Outline each blood parasite and name the species.
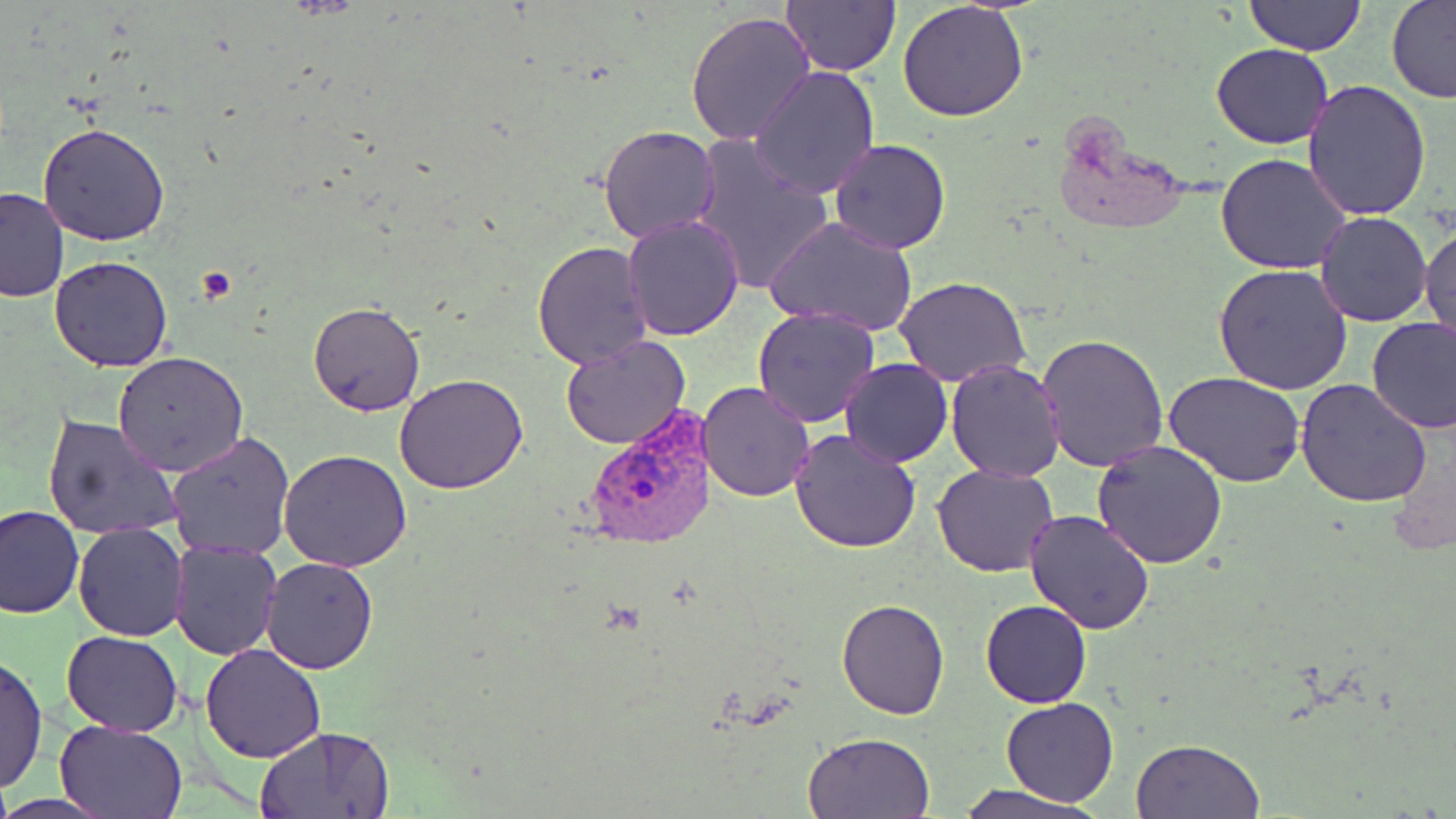
Approximate bounding boxes as [x1, y1, x2, y2] in pixels.
Plasmodium vivax-infected red blood cells: [581, 408, 720, 549].
No Plasmodium falciparum, Plasmodium ovale, Plasmodium malariae, Babesia divergens, or Trypanosoma brucei observed.

Uninfected red blood cell locations: [1244, 0, 1366, 56], [1385, 0, 1456, 104], [780, 1, 901, 75], [898, 1, 1029, 122], [685, 9, 815, 147], [1211, 43, 1335, 149], [749, 65, 879, 199], [1303, 78, 1434, 220], [37, 123, 170, 246], [599, 123, 720, 244], [689, 134, 836, 297], [829, 138, 953, 255], [1215, 154, 1353, 276], [0, 187, 69, 304], [1317, 212, 1432, 327], [624, 214, 745, 339], [764, 215, 921, 336], [1420, 223, 1455, 351], [532, 243, 654, 369], [49, 256, 174, 372], [1212, 263, 1355, 396], [895, 277, 1030, 387], [308, 302, 425, 416], [752, 308, 880, 428], [1367, 317, 1456, 434], [1036, 333, 1169, 472], [560, 336, 692, 451], [711, 344, 866, 484], [113, 352, 248, 476], [839, 358, 952, 468], [945, 359, 1068, 482], [1164, 371, 1305, 488], [395, 374, 528, 494], [1296, 378, 1431, 507], [697, 380, 815, 502], [41, 413, 184, 542], [790, 427, 922, 552], [166, 430, 295, 560], [1092, 441, 1228, 570], [279, 449, 412, 572], [932, 464, 1058, 578], [978, 476, 1123, 618], [1, 504, 84, 618], [1023, 509, 1156, 635], [74, 521, 189, 640], [170, 541, 281, 659], [262, 557, 379, 674], [837, 598, 950, 719], [981, 599, 1092, 707], [61, 631, 183, 736], [201, 645, 327, 764], [1, 653, 47, 796], [1002, 696, 1118, 807], [55, 720, 187, 817], [257, 724, 390, 819], [803, 733, 935, 819], [1129, 737, 1265, 818], [954, 785, 1094, 819]. Platelet locations: [191, 266, 238, 305]. Slide-level diagnosis: Plasmodium vivax. May-Grünwald-Giemsa-stained preparation. Thin blood film. 1000x magnification. Image is 1456×819 pixels. One field of a larger specimen. Optical microscopy.